State the blood parasite species.
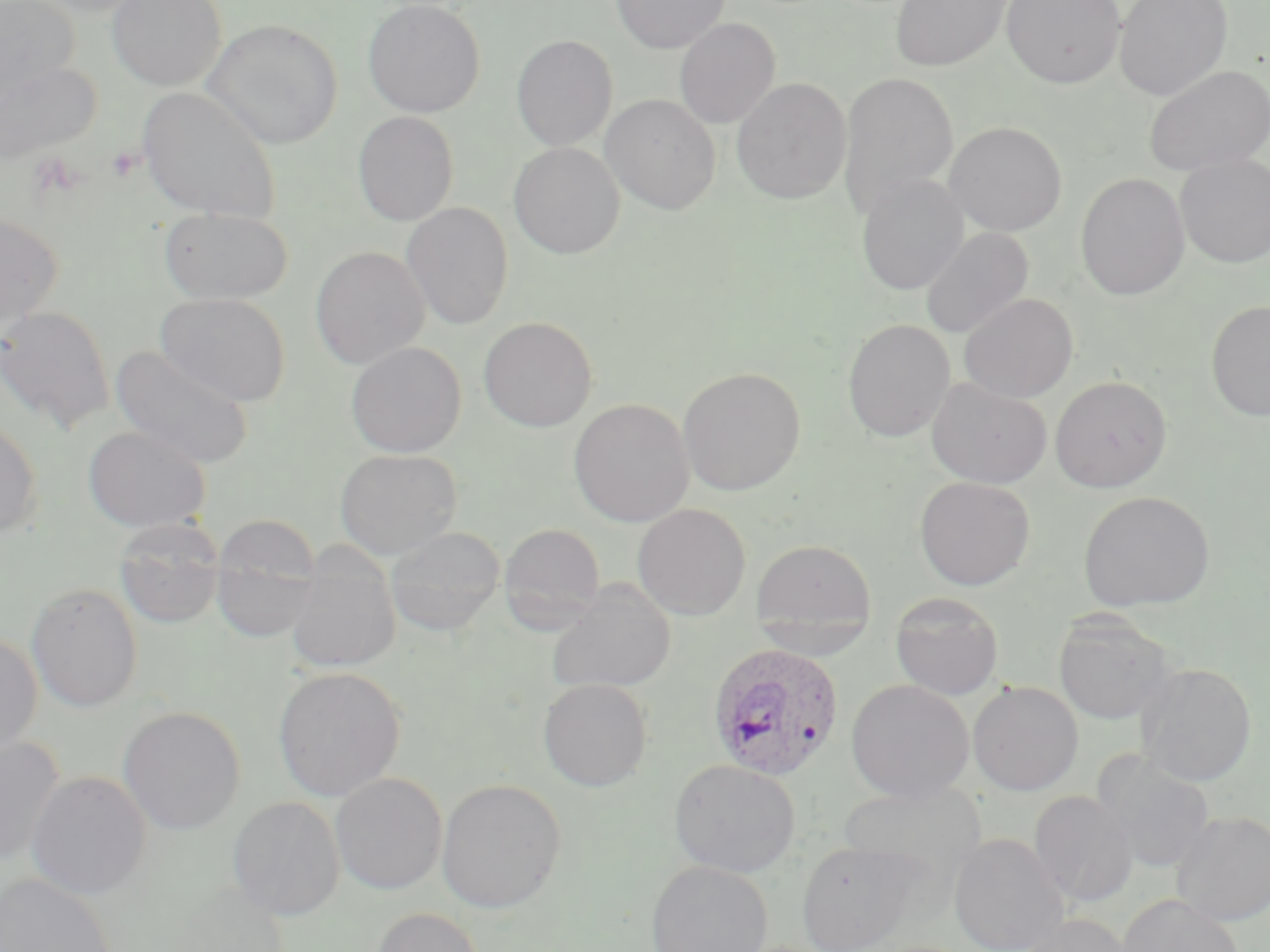

Plasmodium ovale.

modality: light microscopy
stain: May-Grünwald-Giemsa
uninfected_red_blood_cell_locations: 'approximate bounding boxes as named x1/y1/x2/y2 corners in pixels: (x1=1, y1=0, x2=80, y2=100), (x1=107, y1=0, x2=227, y2=90), (x1=363, y1=0, x2=485, y2=117), (x1=611, y1=0, x2=730, y2=53), (x1=890, y1=0, x2=1011, y2=71), (x1=1002, y1=0, x2=1125, y2=88), (x1=1113, y1=0, x2=1233, y2=102), (x1=673, y1=18, x2=780, y2=129), (x1=203, y1=19, x2=342, y2=149), (x1=511, y1=35, x2=617, y2=151), (x1=0, y1=60, x2=100, y2=165), (x1=1144, y1=64, x2=1270, y2=177), (x1=838, y1=71, x2=958, y2=220), (x1=731, y1=77, x2=851, y2=203), (x1=137, y1=87, x2=281, y2=224), (x1=601, y1=94, x2=720, y2=214), (x1=352, y1=111, x2=459, y2=226), (x1=944, y1=121, x2=1068, y2=236), (x1=509, y1=142, x2=625, y2=258), (x1=1174, y1=153, x2=1270, y2=269), (x1=1075, y1=173, x2=1190, y2=301), (x1=856, y1=174, x2=969, y2=295), (x1=400, y1=202, x2=514, y2=330), (x1=158, y1=207, x2=294, y2=305), (x1=0, y1=213, x2=63, y2=330), (x1=920, y1=227, x2=1034, y2=339), (x1=311, y1=246, x2=430, y2=369), (x1=156, y1=292, x2=291, y2=406), (x1=959, y1=292, x2=1078, y2=402), (x1=1205, y1=300, x2=1270, y2=422), (x1=0, y1=305, x2=115, y2=434), (x1=478, y1=317, x2=598, y2=432), (x1=843, y1=318, x2=955, y2=442), (x1=346, y1=341, x2=466, y2=457), (x1=111, y1=345, x2=254, y2=469), (x1=678, y1=366, x2=805, y2=496), (x1=1050, y1=375, x2=1172, y2=492), (x1=926, y1=377, x2=1052, y2=488), (x1=569, y1=398, x2=694, y2=527), (x1=0, y1=416, x2=42, y2=540), (x1=83, y1=424, x2=212, y2=532), (x1=335, y1=448, x2=463, y2=558), (x1=914, y1=475, x2=1036, y2=590), (x1=1078, y1=491, x2=1215, y2=611), (x1=632, y1=503, x2=751, y2=620), (x1=114, y1=520, x2=226, y2=629), (x1=210, y1=521, x2=323, y2=645), (x1=498, y1=523, x2=607, y2=628), (x1=385, y1=526, x2=505, y2=635), (x1=750, y1=537, x2=878, y2=645), (x1=284, y1=555, x2=400, y2=673), (x1=547, y1=581, x2=676, y2=694), (x1=25, y1=582, x2=143, y2=712), (x1=890, y1=591, x2=1004, y2=700), (x1=1053, y1=611, x2=1177, y2=725), (x1=0, y1=631, x2=43, y2=756), (x1=1136, y1=662, x2=1256, y2=787), (x1=273, y1=666, x2=406, y2=801), (x1=538, y1=677, x2=654, y2=792), (x1=846, y1=679, x2=974, y2=802), (x1=968, y1=681, x2=1084, y2=795), (x1=118, y1=706, x2=245, y2=835), (x1=0, y1=735, x2=65, y2=867), (x1=1093, y1=752, x2=1216, y2=873), (x1=668, y1=758, x2=801, y2=877), (x1=25, y1=770, x2=152, y2=900), (x1=330, y1=772, x2=448, y2=894), (x1=436, y1=778, x2=567, y2=913), (x1=837, y1=782, x2=987, y2=880), (x1=1029, y1=790, x2=1138, y2=908), (x1=228, y1=796, x2=345, y2=921), (x1=1171, y1=810, x2=1270, y2=926), (x1=949, y1=832, x2=1069, y2=952), (x1=796, y1=840, x2=925, y2=952), (x1=645, y1=859, x2=773, y2=952), (x1=0, y1=872, x2=116, y2=952), (x1=1117, y1=893, x2=1244, y2=952), (x1=369, y1=907, x2=486, y2=952), (x1=1017, y1=913, x2=1137, y2=952)'
magnification: 1000x
platelet_locations: 'approximate bounding boxes as named x1/y1/x2/y2 corners in pixels: (x1=106, y1=144, x2=144, y2=183)'
field_of_view: single
plasmodium_ovale_infected_red_blood_cell_locations: 'approximate bounding boxes as named x1/y1/x2/y2 corners in pixels: (x1=707, y1=642, x2=845, y2=782)'
preparation: thin blood film
image_size: 1270×952 pixels